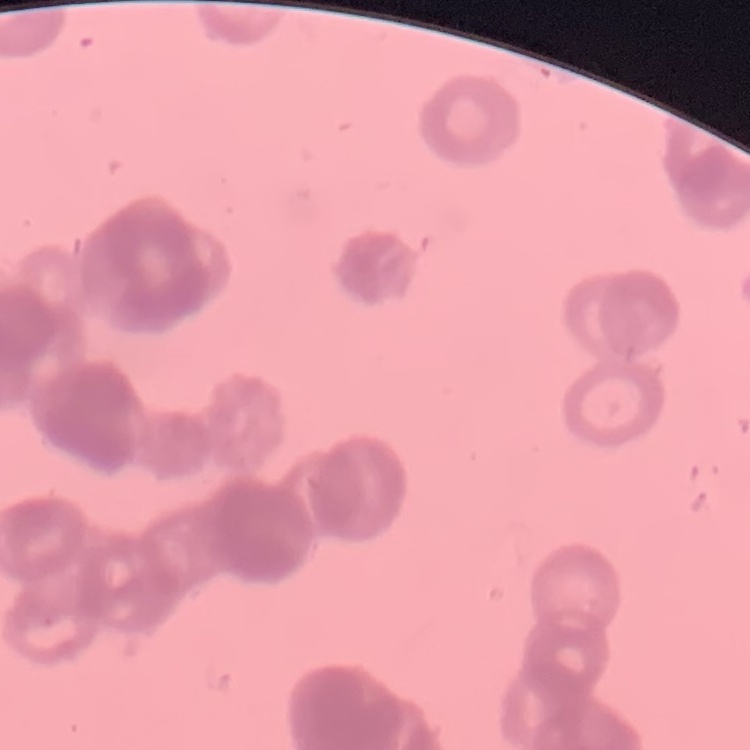
The red blood cells exhibit rouleaux formation. Square crop of a larger photomicrograph. Thin blood film. Field's or Giemsa stain.